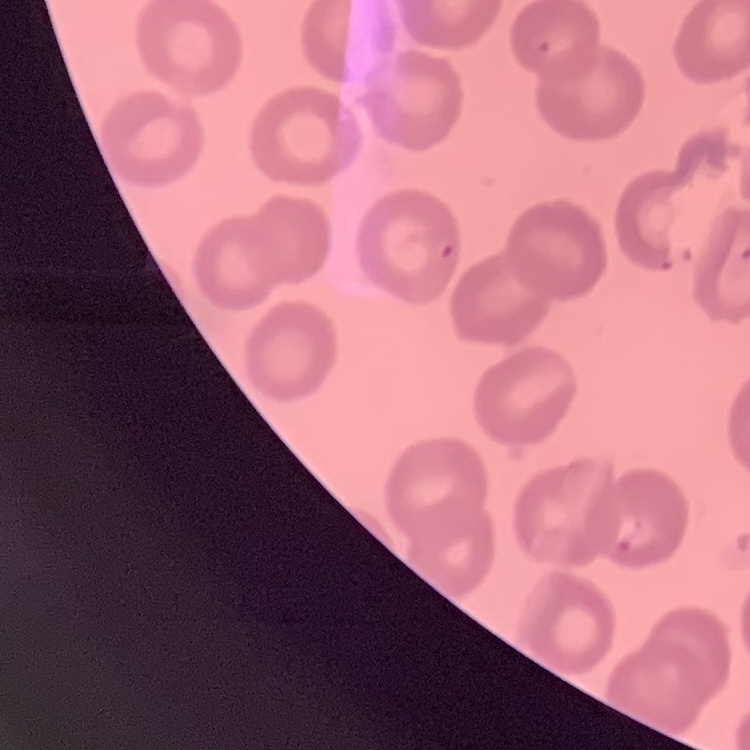
The red blood cells exhibit no rouleaux formation. Thin blood smear. Stained with either Field's or Giemsa. One tile cut from a larger photomicrograph.